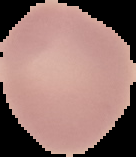
Summary:
  - Image size: 136×157 pixels
  - Preparation: thin blood smear
  - Image type: segmented cell region with the area outside set to black
  - Result: negative for Plasmodium parasites